Describe the morphology of the red blood cells.
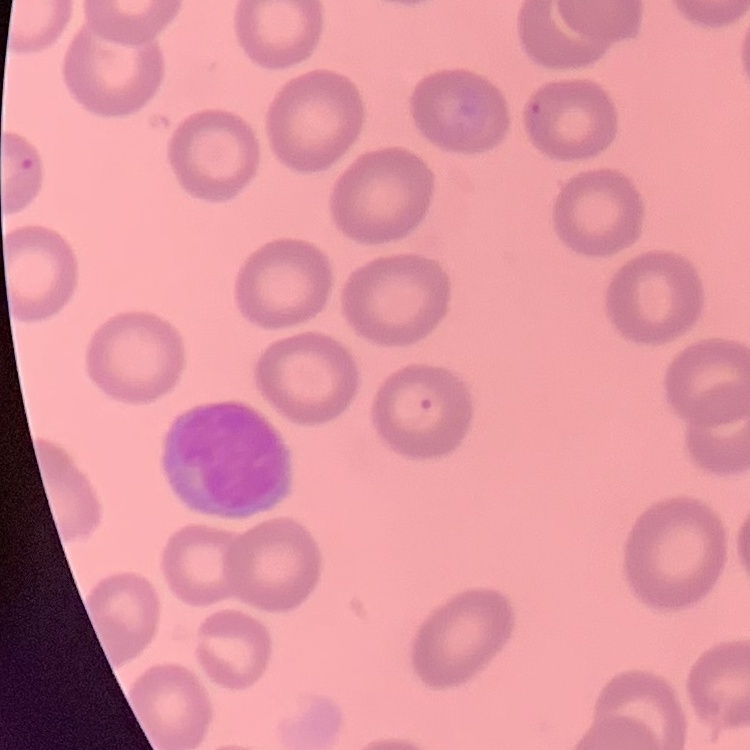

No rouleaux formation.

{
  "stain": "Field's or Giemsa",
  "image_type": "square crop of a larger photomicrograph",
  "preparation": "thin blood film"
}